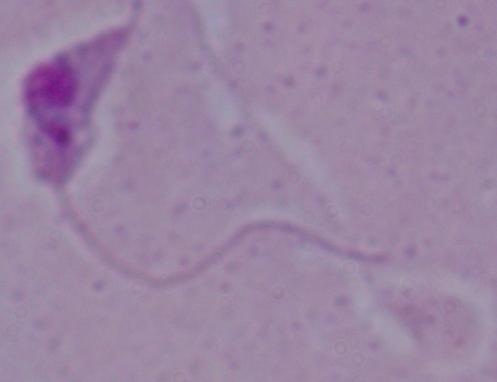

Summary:
  - Modality: micrograph
  - Magnification: 1000x
  - Identification: Leishmania